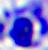 A white blood cell is shown. Captured at 400x magnification. Micrograph.